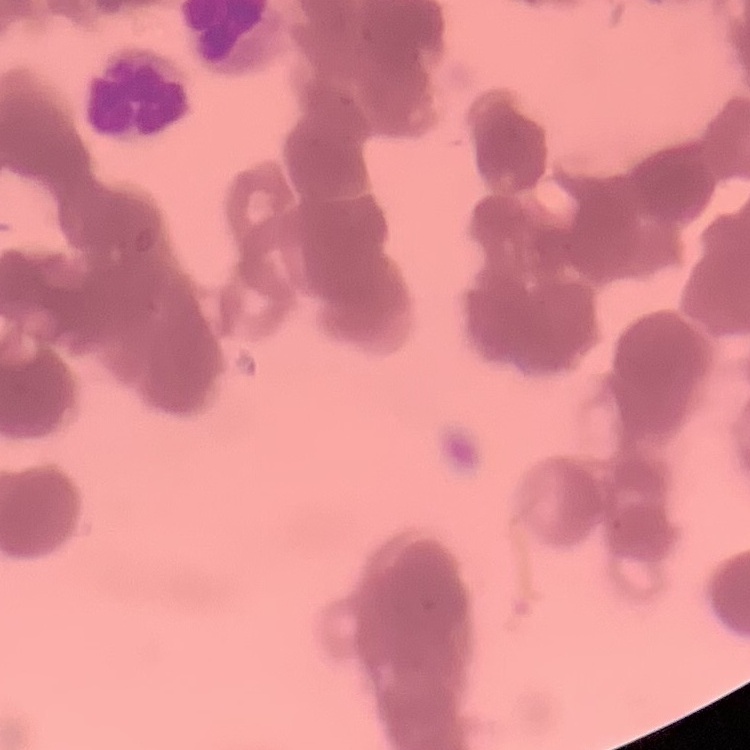

red_blood_cell_morphology: rouleaux formation
image_type: one tile cut from a larger photomicrograph
stain: Field's or Giemsa
preparation: thin peripheral smear